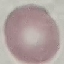

Result: no malaria parasites seen. Acquired by smartphone through the microscope eyepiece. Automatically extracted cell patch, resized to 64 × 64 pixels. Giemsa-stained preparation. Thin smear of blood.